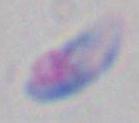 1000x magnification. Toxoplasma gondii is shown. Photomicrograph.